Assess this cell for malaria.
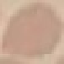
Uninfected.

capture = smartphone camera at the microscope eyepiece
image type = automatically extracted cell patch, resized to 64 × 64 pixels
stain = Giemsa
preparation = thin blood film